Name the parasite shown.
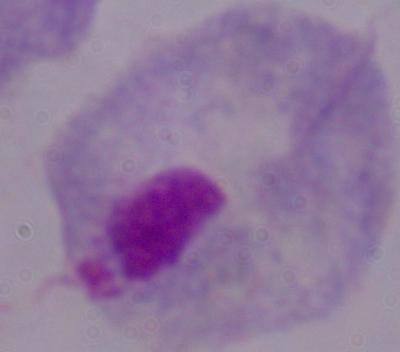
A trichomonad.

Photomicrograph. 1000x magnification.